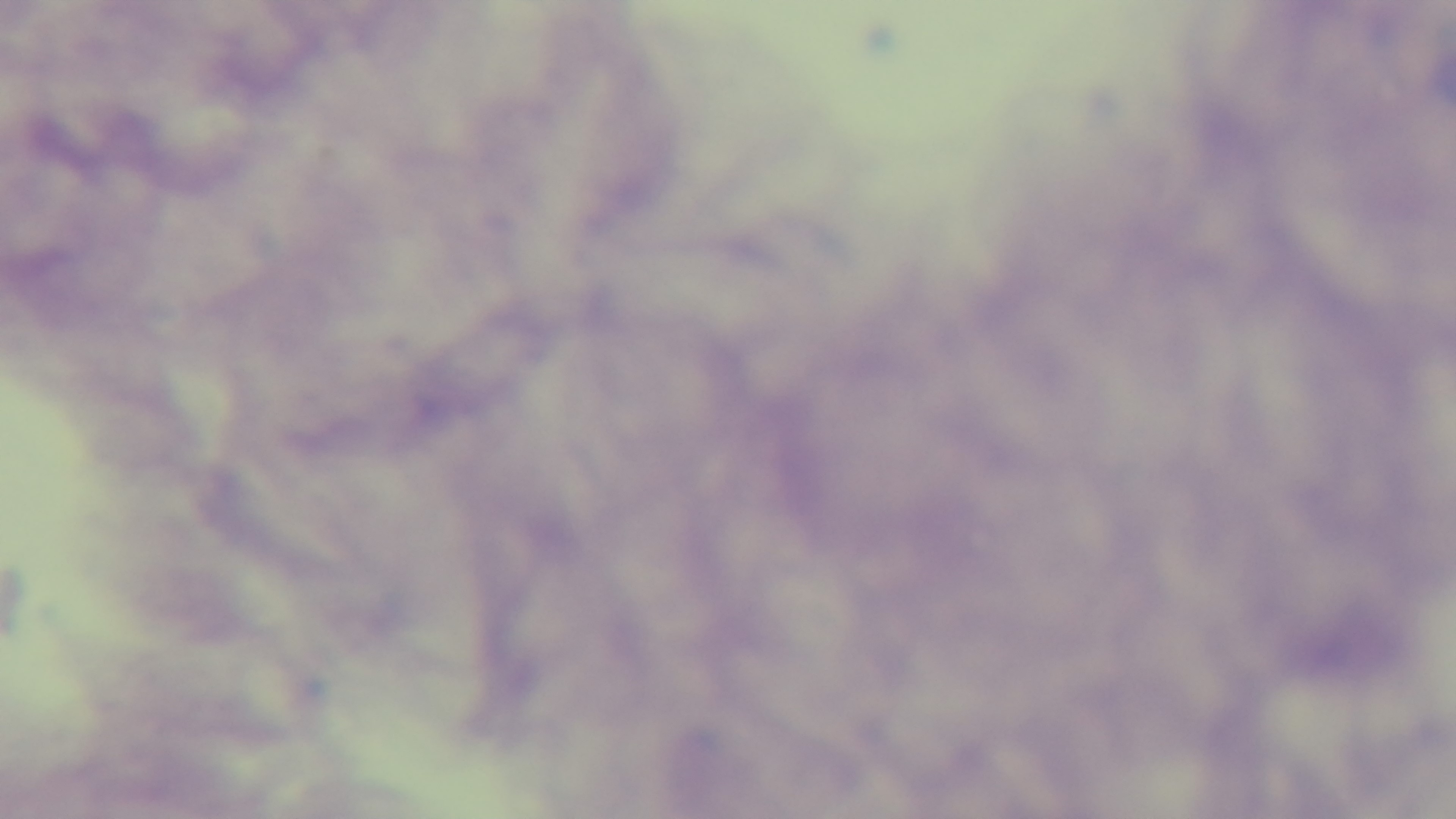

Summary:
  - Stain: Giemsa
  - Preparation: thick smear
  - Objective: 100x oil immersion
  - Modality: light microscopy
  - Field of view: one from the slide
  - Malaria status: uninfected
  - Capture: mounted 4K digital camera